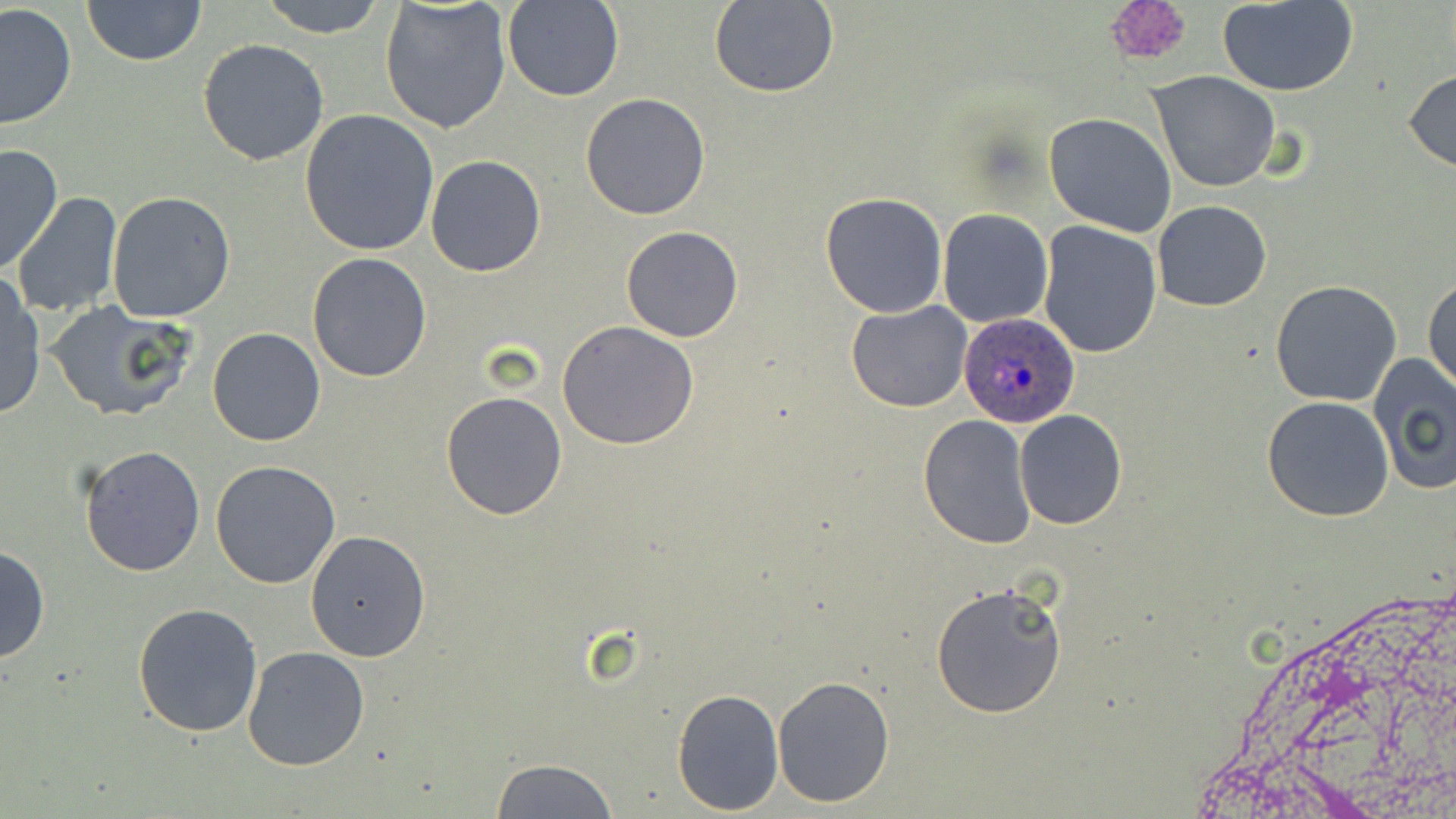

Approximate bounding boxes as (x1,y1)-(x2,y2) corner pairs in pixels. Platelet locations: (1098,0)-(1195,69). Plasmodium ovale-infected red blood cell locations: (960,312)-(1084,428). Uninfected red blood cell locations: (81,0)-(205,66), (256,0)-(390,37), (502,1)-(624,102), (1218,1)-(1359,96), (709,2)-(840,99), (1,3)-(77,132), (379,3)-(513,136), (198,39)-(329,167), (1403,69)-(1456,170), (1148,72)-(1281,193), (580,93)-(710,220), (300,110)-(440,255), (1044,112)-(1177,238), (0,143)-(63,277), (426,155)-(546,277), (107,191)-(237,322), (820,192)-(948,316), (13,193)-(124,320), (1152,200)-(1271,311), (938,208)-(1053,327), (1038,221)-(1163,358), (622,226)-(744,343), (307,253)-(432,381), (0,274)-(45,419), (1424,279)-(1456,391), (1271,281)-(1402,406), (846,300)-(972,414), (44,302)-(200,423), (556,321)-(701,449), (206,327)-(326,446), (1369,353)-(1456,494), (440,390)-(569,520), (1263,395)-(1394,522), (1014,410)-(1127,529), (917,413)-(1036,549), (78,444)-(206,578), (211,459)-(343,589), (305,530)-(431,662), (0,544)-(49,664), (929,581)-(1068,719), (132,601)-(263,738), (241,645)-(369,770), (771,674)-(896,809), (671,687)-(785,815), (492,758)-(620,818). Slide-level diagnosis: Plasmodium ovale. Image is 1456×819 pixels. May-Grünwald-Giemsa stain. Thin blood smear. One field of a larger specimen. Captured at 1000x magnification. Light microscopy.